Classify this cell by malaria status.
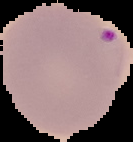

It is parasitized.

Summary:
  - Preparation: thin blood smear
  - Image type: segmented cell region with the area outside set to black
  - Image size: 133×142 pixels